Name the parasite shown.
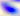
This is Toxoplasma gondii.

Summary:
  - Magnification: 400x
  - Modality: photomicrograph